Report the malaria status of this cell.
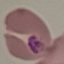
Parasitized.

image_type: automatically extracted cell patch, resized to 64 × 64 pixels
capture: smartphone through the microscope eyepiece
preparation: thin blood smear
stain: Giemsa